Comment on the morphology of the erythrocytes.
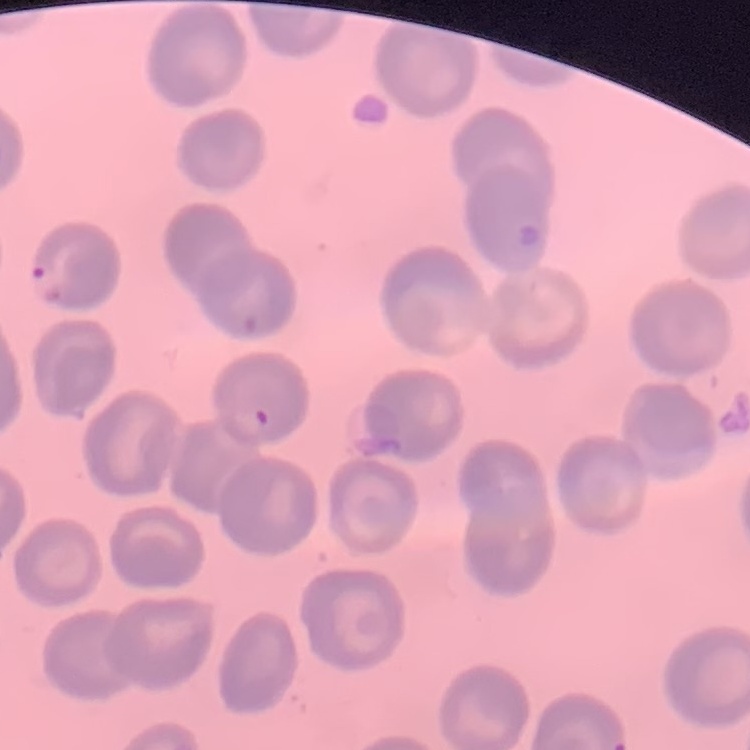
They show no rouleaux formation.

Thin peripheral smear. Stained with either Field's or Giemsa. One tile cut from a larger photomicrograph.